State which parasite is depicted.
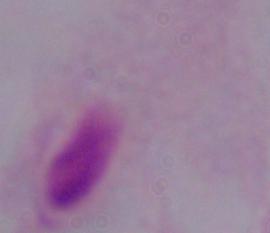
A trichomonad.

Captured at 1000x magnification. Micrograph.